Locate and identify every blood parasite.
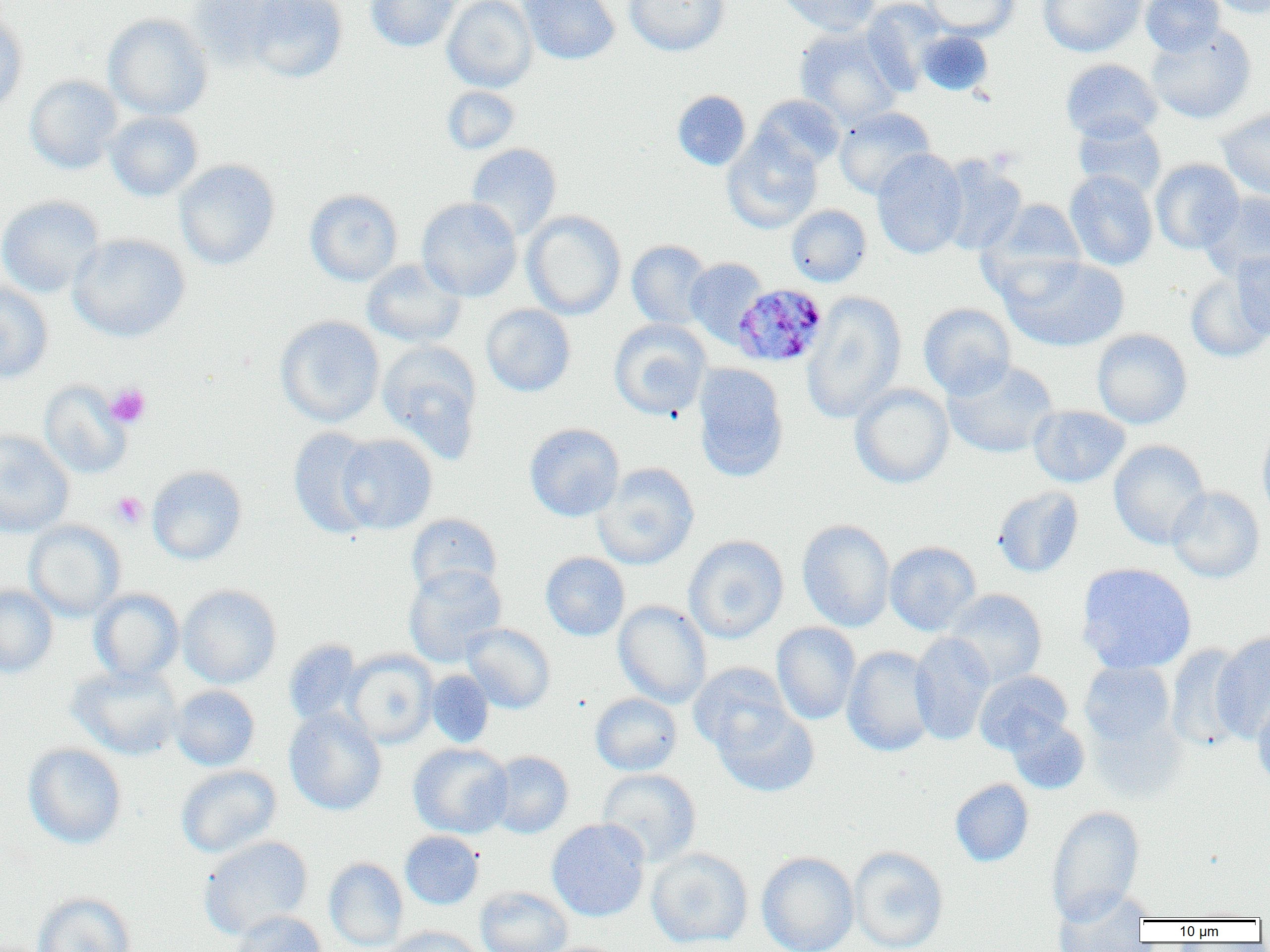
Approximate bounding boxes as (x1, y1, x2, y2) in pixels.
Plasmodium malariae-infected red blood cells: (732, 283, 829, 367).
No Plasmodium falciparum, Plasmodium ovale, Plasmodium vivax, Babesia divergens, or Trypanosoma brucei observed.

slide-level diagnosis = Plasmodium malariae
modality = optical microscopy
uninfected red blood cell locations = approximate bounding boxes as (x1, y1, x2, y2) in pixels: (188, 0, 311, 68), (242, 0, 349, 83), (365, 0, 460, 52), (442, 0, 537, 92), (519, 0, 620, 65), (623, 0, 730, 56), (776, 0, 880, 36), (861, 0, 948, 94), (922, 0, 1019, 40), (1038, 0, 1146, 57), (1141, 0, 1225, 56), (1207, 0, 1269, 19), (0, 10, 28, 116), (104, 13, 213, 120), (1146, 24, 1256, 124), (794, 25, 904, 130), (917, 31, 993, 95), (1060, 59, 1162, 143), (25, 74, 124, 174), (442, 86, 520, 154), (672, 90, 751, 170), (752, 94, 846, 172), (834, 106, 936, 199), (1217, 107, 1270, 201), (106, 111, 203, 201), (1072, 116, 1167, 199), (722, 132, 823, 233), (465, 143, 562, 240), (871, 149, 968, 259), (936, 155, 1028, 256), (174, 159, 280, 270), (1150, 159, 1244, 254), (1064, 170, 1158, 271), (305, 189, 403, 286), (1200, 190, 1270, 282), (304, 193, 523, 289), (0, 195, 105, 298), (416, 197, 522, 301), (980, 198, 1087, 289), (786, 204, 871, 287), (522, 210, 626, 320), (68, 233, 190, 342), (626, 240, 714, 330), (1232, 251, 1270, 340), (1001, 255, 1129, 352), (685, 257, 769, 347), (361, 259, 466, 348), (1185, 274, 1270, 362), (0, 281, 53, 384), (802, 291, 907, 424), (918, 303, 1016, 399), (481, 304, 576, 397), (275, 316, 385, 427), (609, 318, 711, 420), (1091, 328, 1192, 429), (377, 341, 483, 462), (943, 360, 1058, 459), (693, 363, 789, 481), (39, 381, 132, 479), (850, 383, 954, 488), (1029, 406, 1130, 488), (1257, 419, 1270, 522), (524, 423, 625, 521), (288, 427, 383, 538), (0, 430, 75, 538), (336, 434, 437, 534), (1108, 440, 1210, 549), (594, 463, 698, 569), (147, 465, 247, 565), (993, 485, 1084, 578), (1166, 486, 1265, 583), (406, 513, 503, 598), (796, 519, 896, 632), (24, 520, 126, 621), (683, 535, 789, 644), (885, 541, 981, 636), (541, 552, 629, 641), (1076, 563, 1197, 674), (404, 564, 507, 667), (0, 584, 58, 678), (177, 584, 282, 688), (89, 588, 184, 684), (944, 588, 1047, 688), (613, 600, 712, 708), (771, 622, 861, 725), (461, 623, 556, 713), (1211, 631, 1270, 743), (909, 632, 996, 745), (284, 639, 365, 728), (1165, 643, 1251, 750), (842, 645, 938, 756), (343, 650, 438, 747), (1079, 661, 1176, 748), (689, 663, 792, 754), (68, 664, 183, 761), (426, 670, 494, 747), (974, 670, 1072, 754), (170, 685, 260, 770), (590, 693, 682, 775), (1252, 693, 1270, 790), (714, 705, 820, 797), (284, 707, 387, 815), (1085, 711, 1189, 804), (1006, 715, 1090, 794), (23, 743, 127, 848), (408, 743, 512, 838), (486, 751, 573, 838), (175, 765, 282, 858), (597, 769, 701, 867), (950, 778, 1034, 867), (1046, 805, 1145, 924), (547, 818, 650, 922), (400, 830, 484, 909), (198, 835, 313, 939), (848, 846, 949, 952), (646, 847, 754, 949), (757, 851, 859, 952), (324, 857, 408, 951), (475, 886, 573, 952), (1053, 887, 1152, 951), (33, 892, 137, 952), (228, 909, 329, 952), (383, 925, 485, 952)
preparation = thin blood film
platelet locations = approximate bounding boxes as (x1, y1, x2, y2) in pixels: (105, 384, 151, 428), (112, 491, 147, 528)
magnification = 1000x
field of view = single
image size = 1270×952 pixels